Locate every Plasmodium malariae-infected red blood cell.
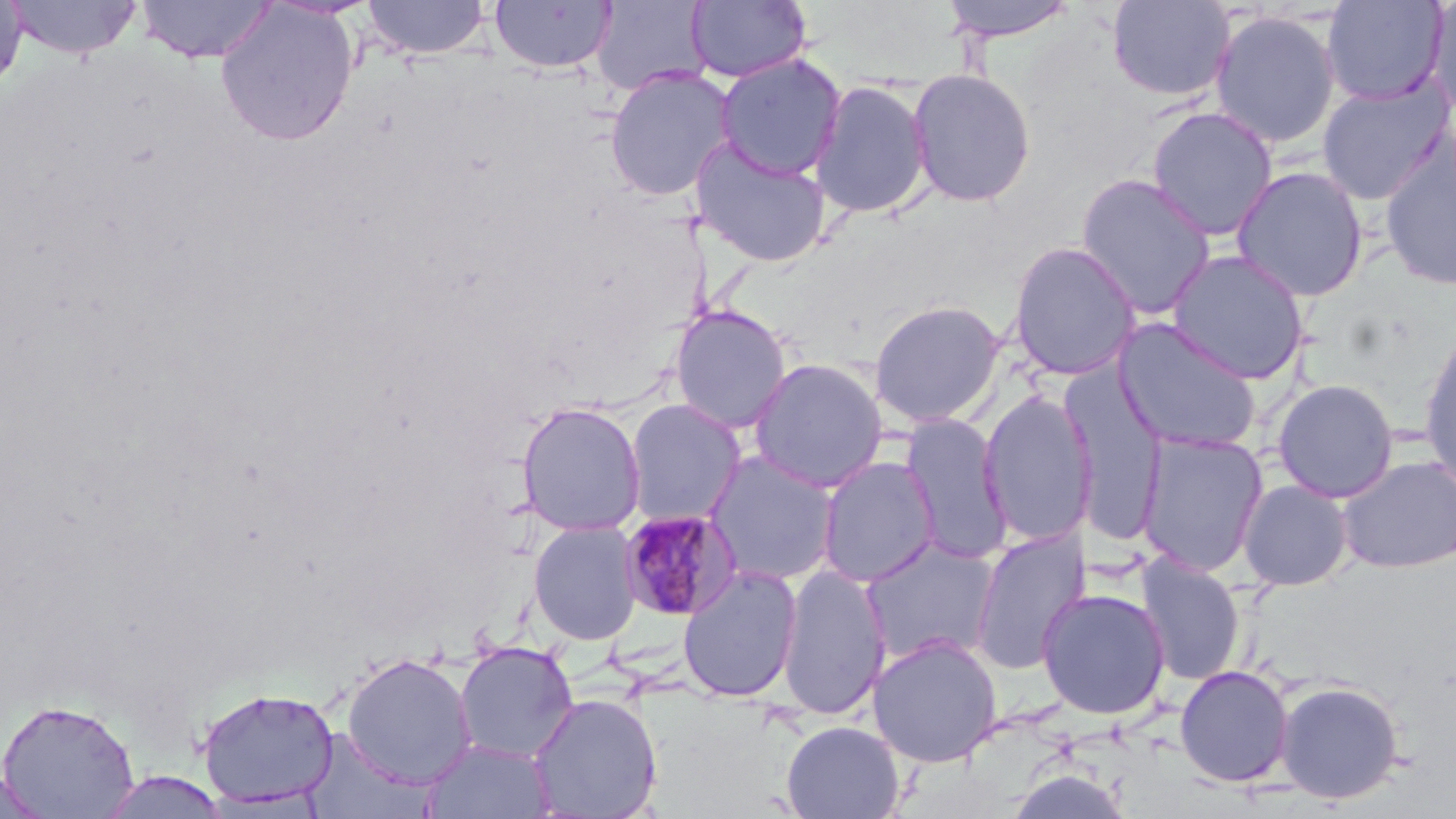

Approximate bounding boxes as named x1/y1/x2/y2 corners in pixels.
Plasmodium malariae-infected red blood cells: (x1=617, y1=509, x2=743, y2=622).

{
  "slide_level_diagnosis": "Plasmodium malariae",
  "field_of_view": "one of a larger specimen",
  "stain": "May-Grünwald-Giemsa",
  "magnification": "1000x",
  "image_size": "1456×819 pixels",
  "uninfected_red_blood_cell_locations": "approximate bounding boxes as named x1/y1/x2/y2 corners in pixels: (x1=5, y1=0, x2=144, y2=60), (x1=136, y1=0, x2=277, y2=63), (x1=139, y1=0, x2=318, y2=106), (x1=361, y1=0, x2=492, y2=60), (x1=490, y1=0, x2=617, y2=74), (x1=936, y1=0, x2=1082, y2=43), (x1=1107, y1=0, x2=1235, y2=102), (x1=1321, y1=0, x2=1449, y2=106), (x1=1426, y1=0, x2=1456, y2=121), (x1=0, y1=1, x2=29, y2=96), (x1=590, y1=1, x2=713, y2=96), (x1=687, y1=1, x2=811, y2=83), (x1=216, y1=2, x2=359, y2=146), (x1=1209, y1=10, x2=1341, y2=149), (x1=715, y1=52, x2=846, y2=180), (x1=604, y1=66, x2=736, y2=201), (x1=907, y1=68, x2=1036, y2=207), (x1=1316, y1=78, x2=1454, y2=205), (x1=810, y1=79, x2=932, y2=220), (x1=1146, y1=105, x2=1279, y2=242), (x1=691, y1=136, x2=832, y2=268), (x1=1378, y1=138, x2=1456, y2=292), (x1=1231, y1=165, x2=1369, y2=302), (x1=1075, y1=173, x2=1216, y2=320), (x1=1007, y1=241, x2=1142, y2=381), (x1=1166, y1=249, x2=1309, y2=383), (x1=868, y1=299, x2=1005, y2=428), (x1=669, y1=305, x2=792, y2=433), (x1=1111, y1=317, x2=1262, y2=453), (x1=1419, y1=332, x2=1456, y2=491), (x1=749, y1=357, x2=888, y2=492), (x1=1272, y1=378, x2=1399, y2=503), (x1=1066, y1=381, x2=1169, y2=545), (x1=978, y1=390, x2=1096, y2=547), (x1=624, y1=398, x2=746, y2=527), (x1=516, y1=401, x2=647, y2=537), (x1=899, y1=413, x2=1012, y2=564), (x1=1137, y1=431, x2=1269, y2=577), (x1=703, y1=450, x2=840, y2=586), (x1=817, y1=455, x2=940, y2=588), (x1=1336, y1=455, x2=1456, y2=574), (x1=1238, y1=478, x2=1354, y2=591), (x1=528, y1=520, x2=642, y2=645), (x1=971, y1=528, x2=1090, y2=675), (x1=861, y1=537, x2=1001, y2=667), (x1=1136, y1=553, x2=1246, y2=686), (x1=677, y1=564, x2=803, y2=702), (x1=777, y1=564, x2=891, y2=720), (x1=1036, y1=588, x2=1170, y2=720), (x1=867, y1=634, x2=1003, y2=767), (x1=453, y1=641, x2=579, y2=762), (x1=342, y1=652, x2=477, y2=789), (x1=1174, y1=664, x2=1294, y2=788), (x1=1274, y1=679, x2=1406, y2=805), (x1=197, y1=685, x2=339, y2=809), (x1=529, y1=692, x2=663, y2=819), (x1=0, y1=698, x2=140, y2=817), (x1=781, y1=720, x2=905, y2=819), (x1=302, y1=731, x2=436, y2=819), (x1=423, y1=739, x2=555, y2=819), (x1=1, y1=768, x2=53, y2=817), (x1=97, y1=770, x2=230, y2=818)",
  "modality": "light microscopy",
  "preparation": "thin blood smear"
}